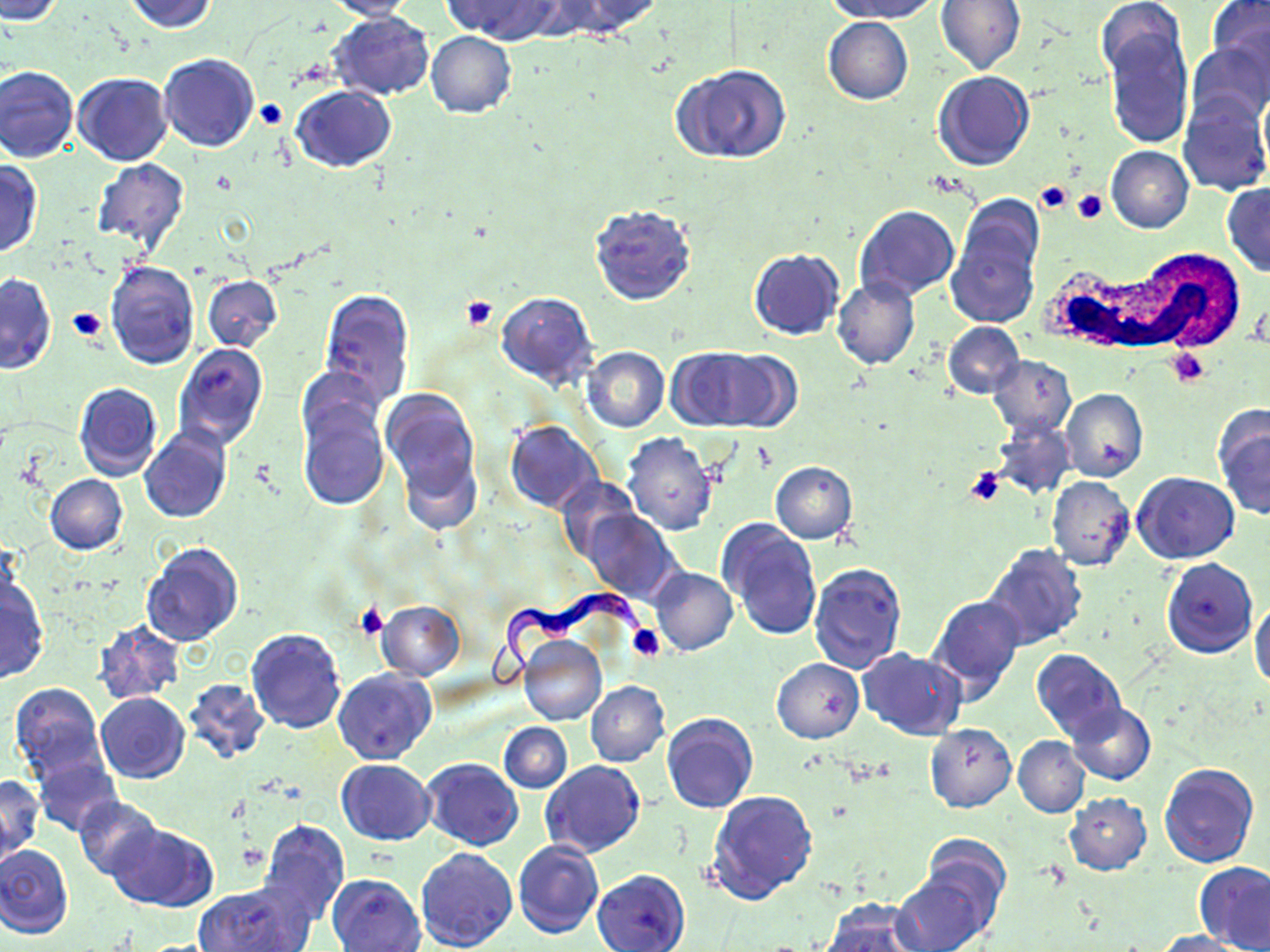

slide-level diagnosis = Trypanosoma brucei
field of view = one of a larger specimen
magnification = 1000x
uninfected red blood cell locations = approximate bounding boxes as named x1/y1/x2/y2 corners in pixels: (x1=0, y1=0, x2=67, y2=24), (x1=123, y1=0, x2=220, y2=34), (x1=443, y1=0, x2=558, y2=42), (x1=554, y1=0, x2=662, y2=38), (x1=822, y1=0, x2=942, y2=23), (x1=935, y1=0, x2=1026, y2=74), (x1=1205, y1=0, x2=1270, y2=81), (x1=324, y1=1, x2=419, y2=21), (x1=1097, y1=2, x2=1189, y2=87), (x1=328, y1=10, x2=435, y2=101), (x1=823, y1=16, x2=913, y2=105), (x1=1101, y1=24, x2=1193, y2=150), (x1=425, y1=32, x2=517, y2=118), (x1=1185, y1=39, x2=1270, y2=126), (x1=158, y1=53, x2=260, y2=152), (x1=673, y1=63, x2=790, y2=164), (x1=1, y1=65, x2=80, y2=164), (x1=932, y1=71, x2=1034, y2=172), (x1=73, y1=72, x2=172, y2=165), (x1=292, y1=86, x2=396, y2=173), (x1=1178, y1=96, x2=1270, y2=195), (x1=1105, y1=145, x2=1193, y2=233), (x1=91, y1=159, x2=189, y2=252), (x1=0, y1=161, x2=43, y2=258), (x1=1222, y1=183, x2=1270, y2=276), (x1=589, y1=204, x2=697, y2=305), (x1=854, y1=206, x2=960, y2=302), (x1=946, y1=212, x2=1042, y2=328), (x1=749, y1=249, x2=844, y2=340), (x1=106, y1=260, x2=199, y2=368), (x1=0, y1=274, x2=56, y2=375), (x1=203, y1=275, x2=282, y2=352), (x1=832, y1=278, x2=921, y2=369), (x1=318, y1=289, x2=414, y2=405), (x1=496, y1=290, x2=598, y2=390), (x1=943, y1=322, x2=1024, y2=400), (x1=173, y1=344, x2=268, y2=450), (x1=582, y1=346, x2=670, y2=431), (x1=669, y1=348, x2=774, y2=430), (x1=987, y1=355, x2=1075, y2=438), (x1=297, y1=366, x2=382, y2=446), (x1=74, y1=383, x2=162, y2=481), (x1=379, y1=388, x2=479, y2=500), (x1=1060, y1=388, x2=1148, y2=481), (x1=296, y1=396, x2=388, y2=509), (x1=1213, y1=405, x2=1270, y2=521), (x1=505, y1=421, x2=603, y2=513), (x1=991, y1=422, x2=1076, y2=499), (x1=139, y1=428, x2=231, y2=524), (x1=623, y1=432, x2=718, y2=535), (x1=400, y1=449, x2=482, y2=534), (x1=770, y1=461, x2=858, y2=544), (x1=1132, y1=472, x2=1238, y2=563), (x1=45, y1=474, x2=127, y2=555), (x1=554, y1=476, x2=640, y2=561), (x1=1046, y1=476, x2=1135, y2=571), (x1=581, y1=510, x2=682, y2=603), (x1=717, y1=519, x2=821, y2=641), (x1=141, y1=541, x2=244, y2=647), (x1=982, y1=542, x2=1088, y2=650), (x1=1162, y1=557, x2=1257, y2=658), (x1=808, y1=562, x2=908, y2=672), (x1=650, y1=566, x2=738, y2=656), (x1=0, y1=578, x2=48, y2=684), (x1=927, y1=594, x2=1027, y2=703), (x1=1250, y1=599, x2=1270, y2=692), (x1=377, y1=600, x2=465, y2=680), (x1=91, y1=621, x2=185, y2=704), (x1=247, y1=627, x2=345, y2=732), (x1=518, y1=634, x2=606, y2=726), (x1=1031, y1=648, x2=1127, y2=743), (x1=859, y1=649, x2=967, y2=739), (x1=772, y1=658, x2=864, y2=743), (x1=333, y1=669, x2=436, y2=765), (x1=182, y1=678, x2=271, y2=764), (x1=585, y1=681, x2=670, y2=767), (x1=10, y1=683, x2=106, y2=777), (x1=96, y1=693, x2=190, y2=783), (x1=1066, y1=703, x2=1156, y2=786), (x1=661, y1=713, x2=758, y2=815), (x1=499, y1=723, x2=571, y2=791), (x1=925, y1=723, x2=1016, y2=812), (x1=1013, y1=735, x2=1088, y2=817), (x1=32, y1=755, x2=122, y2=836), (x1=420, y1=758, x2=522, y2=851), (x1=335, y1=759, x2=435, y2=845), (x1=541, y1=760, x2=645, y2=858), (x1=1160, y1=762, x2=1260, y2=868), (x1=0, y1=774, x2=43, y2=857), (x1=706, y1=789, x2=818, y2=907), (x1=1063, y1=794, x2=1152, y2=875), (x1=73, y1=796, x2=162, y2=878), (x1=258, y1=819, x2=349, y2=926), (x1=109, y1=824, x2=218, y2=912), (x1=921, y1=836, x2=1011, y2=931), (x1=513, y1=840, x2=604, y2=939), (x1=0, y1=845, x2=73, y2=939), (x1=416, y1=848, x2=518, y2=952), (x1=1194, y1=862, x2=1270, y2=952), (x1=592, y1=869, x2=690, y2=952), (x1=891, y1=871, x2=992, y2=952), (x1=327, y1=873, x2=424, y2=952), (x1=194, y1=879, x2=314, y2=952), (x1=819, y1=898, x2=927, y2=952), (x1=1152, y1=930, x2=1248, y2=952)
modality = optical microscopy
white blood cell locations = approximate bounding boxes as named x1/y1/x2/y2 corners in pixels: (x1=1047, y1=249, x2=1240, y2=363)
stain = May-Grünwald-Giemsa
platelet locations = approximate bounding boxes as named x1/y1/x2/y2 corners in pixels: (x1=255, y1=98, x2=287, y2=128), (x1=1035, y1=181, x2=1073, y2=215), (x1=1073, y1=188, x2=1109, y2=224), (x1=462, y1=296, x2=498, y2=329), (x1=66, y1=306, x2=108, y2=343), (x1=1166, y1=347, x2=1209, y2=386), (x1=964, y1=465, x2=1008, y2=505), (x1=357, y1=605, x2=388, y2=639), (x1=627, y1=625, x2=665, y2=661)
image size = 1270×952 pixels
Trypanosoma brucei locations = approximate bounding boxes as named x1/y1/x2/y2 corners in pixels: (x1=480, y1=590, x2=651, y2=689)
preparation = thin blood film